Describe the morphology of the erythrocytes.
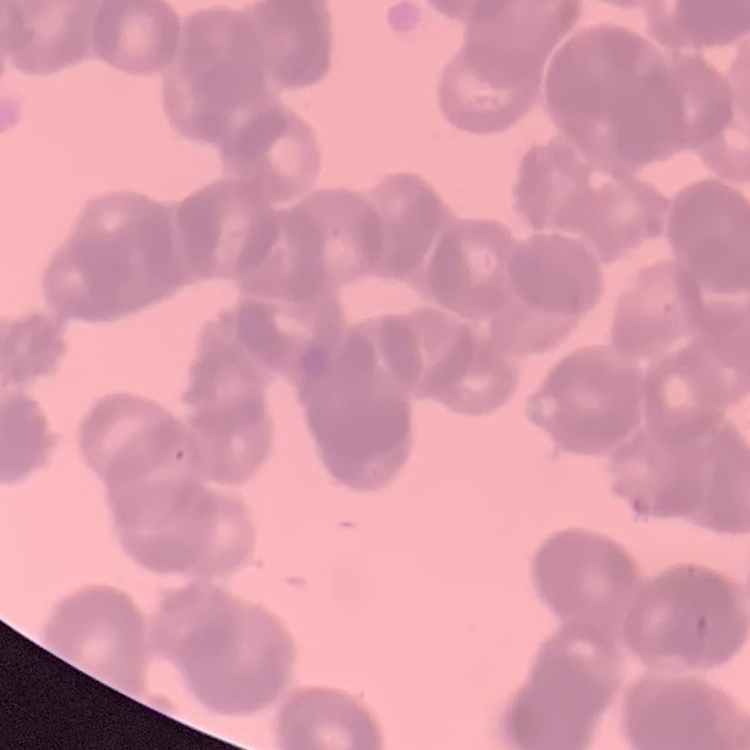

Rouleaux formation.

Stained with either Field's or Giemsa. Square crop of a larger photomicrograph. Thin blood smear.